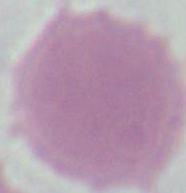

Summary:
  - Magnification: 1000x
  - Modality: micrograph
  - Identification: erythrocyte